Outline platelets.
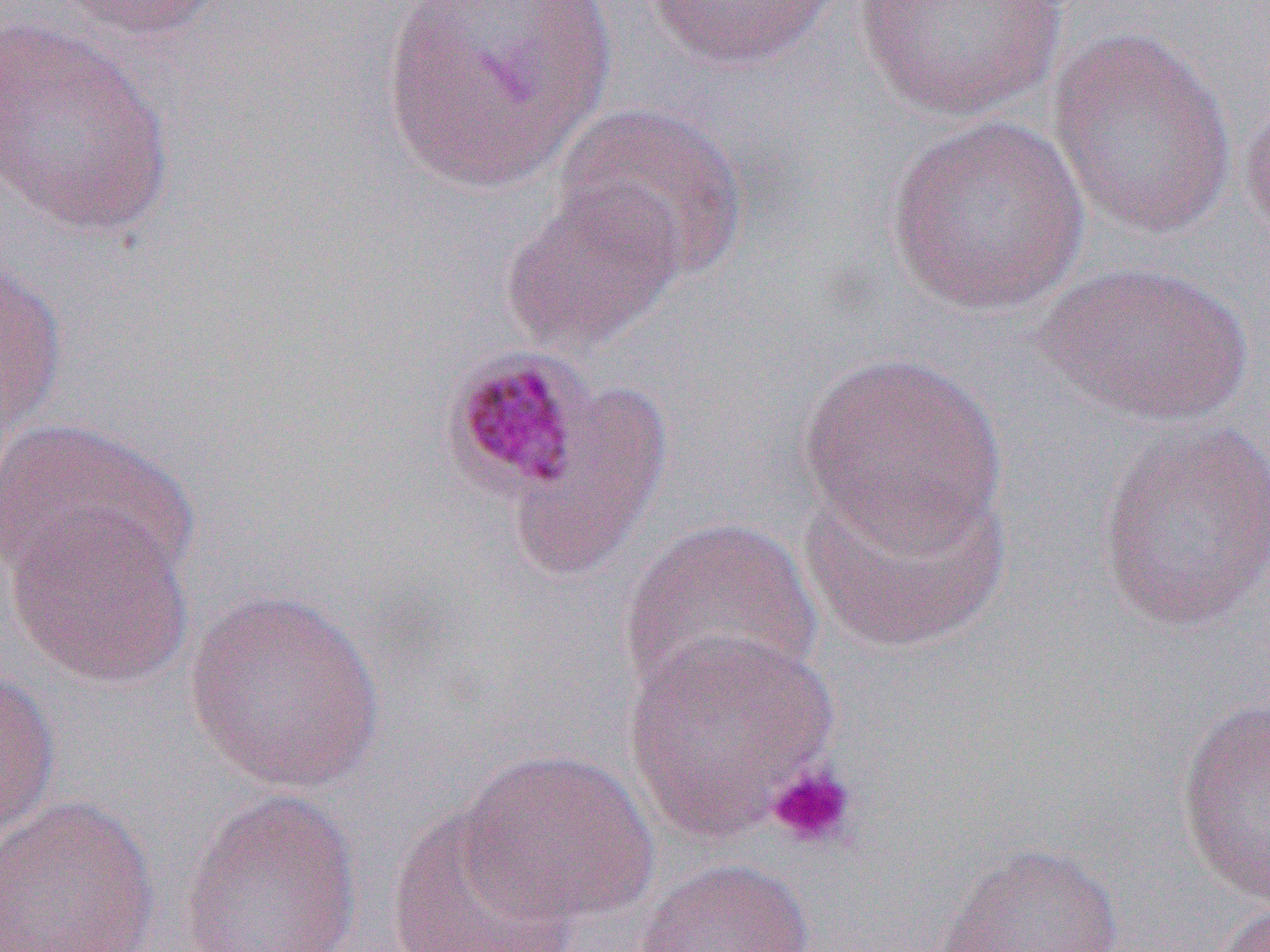

Approximate bounding boxes as (x1,y1)-(x2,y2) corner pairs in pixels.
Platelets (subset): (764,763)-(859,850).

{
  "slide_level_diagnosis": "Plasmodium malariae",
  "magnification": "1000x",
  "image_size": "1270×952 pixels",
  "modality": "light microscopy",
  "uninfected_red_blood_cell_locations_subset": "approximate bounding boxes as (x1,y1)-(x2,y2) corner pairs in pixels: (56,0)-(224,41), (378,0)-(616,192), (643,0)-(840,72), (852,0)-(1071,123), (0,17)-(176,239), (1046,27)-(1238,241), (1238,93)-(1270,251), (551,102)-(749,282), (884,115)-(1092,315), (498,181)-(686,356), (0,255)-(68,450), (1037,261)-(1254,427), (798,350)-(1007,552), (503,381)-(673,585), (0,417)-(197,594), (1095,418)-(1270,633), (799,467)-(1011,655), (4,503)-(195,690), (619,516)-(824,707), (181,588)-(387,795), (623,627)-(839,840), (0,665)-(62,843), (1175,695)-(1270,906), (459,748)-(659,927), (178,787)-(364,952), (0,795)-(161,952), (382,806)-(578,951), (927,842)-(1125,951), (632,856)-(817,952), (1207,901)-(1270,952)",
  "field_of_view": "single",
  "preparation": "thin blood film"
}